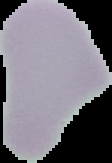

{
  "image_size": "112×163 pixels",
  "malaria_status": "uninfected",
  "image_type": "segmented cell region with the area outside set to black",
  "preparation": "thin blood film"
}